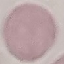
Summary:
  - Result: no malaria parasites seen
  - Image type: cell patch, automatically extracted from a larger field of view and resized to 64 × 64 pixels
  - Stain: Giemsa
  - Preparation: thin smear
  - Capture: smartphone through the microscope eyepiece